Name the blood parasite species.
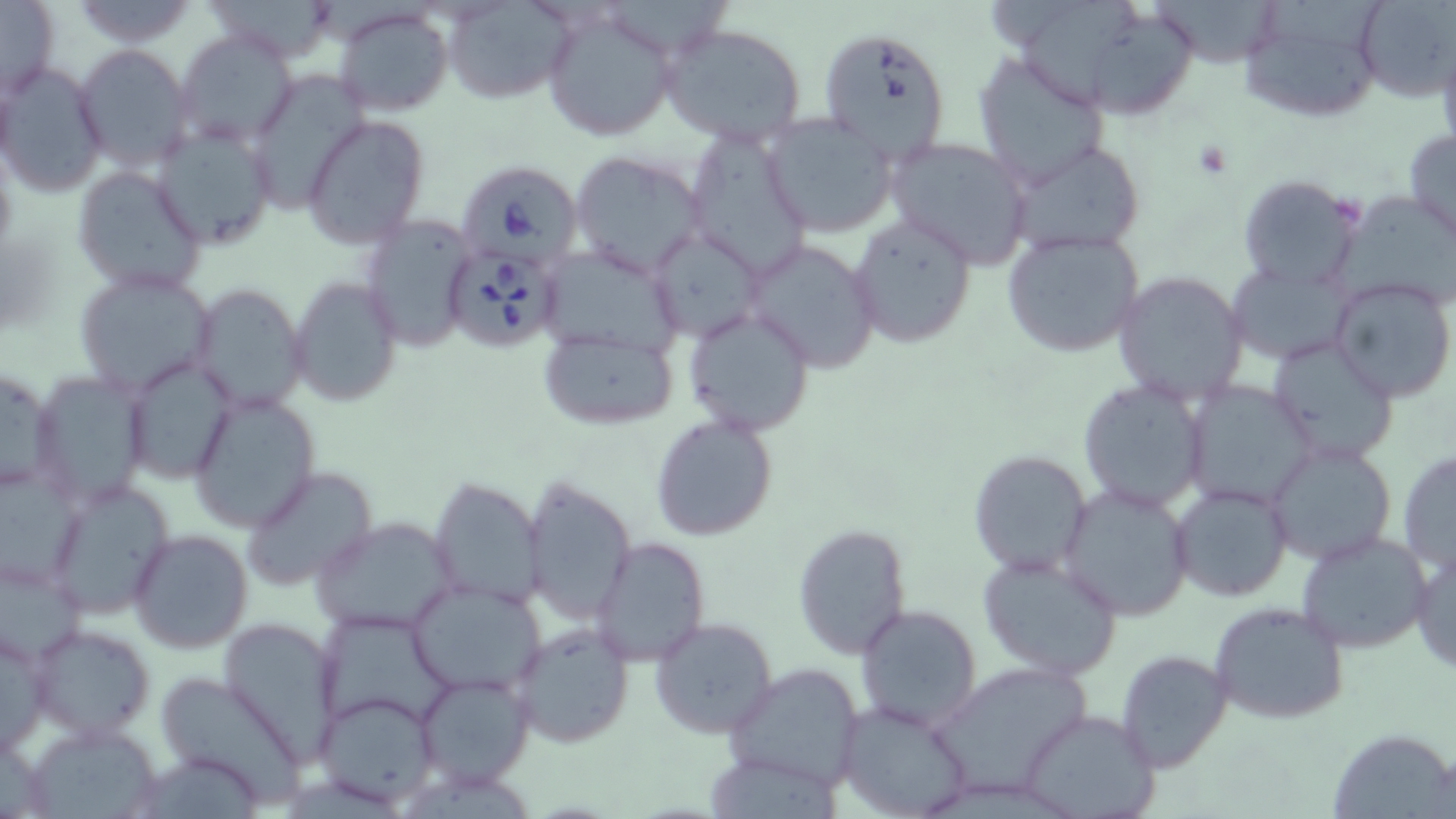
Babesia divergens.

Approximate bounding boxes as (x1,y1)-(x2,y2) corner pairs in pixels. Uninfected red blood cell locations: (204,0)-(334,64), (1145,0)-(1289,68), (1354,0)-(1453,102), (1,1)-(59,100), (68,1)-(199,48), (443,1)-(576,103), (1238,1)-(1391,124), (1026,3)-(1144,110), (542,5)-(679,142), (334,6)-(452,115), (1091,20)-(1194,118), (661,22)-(807,147), (816,24)-(951,161), (174,30)-(302,150), (1437,31)-(1456,167), (73,44)-(192,171), (973,52)-(1109,188), (0,61)-(108,198), (246,72)-(369,214), (761,114)-(896,238), (303,115)-(430,251), (151,120)-(277,249), (684,128)-(811,281), (1404,128)-(1456,243), (885,136)-(1032,267), (1010,139)-(1146,256), (570,149)-(709,276), (73,166)-(205,295), (1234,174)-(1364,293), (1337,190)-(1456,310), (359,212)-(478,353), (846,214)-(979,349), (648,226)-(765,342), (1002,229)-(1145,358), (742,239)-(883,373), (538,243)-(682,362), (1227,259)-(1354,368), (73,268)-(216,396), (1112,270)-(1249,406), (289,275)-(403,406), (1329,275)-(1456,405), (190,284)-(308,411), (683,306)-(816,437), (537,326)-(679,430), (1267,335)-(1402,464), (122,355)-(237,484), (0,363)-(60,497), (32,369)-(151,509), (1078,379)-(1210,513), (1184,380)-(1318,508), (186,389)-(322,533), (649,412)-(779,540), (1265,441)-(1398,568), (1397,448)-(1456,574), (967,449)-(1092,573), (0,462)-(86,592), (242,464)-(378,593), (522,475)-(635,624), (428,477)-(545,606), (44,478)-(174,618), (1169,481)-(1294,604), (1056,482)-(1196,621), (312,516)-(459,637), (794,523)-(911,658), (128,529)-(254,653), (1297,529)-(1434,655), (590,537)-(712,667), (1410,546)-(1456,675), (0,550)-(89,667), (977,551)-(1123,681), (408,580)-(548,696), (1208,601)-(1350,725), (854,604)-(982,731), (315,608)-(455,735), (219,616)-(344,759), (649,616)-(779,741), (510,621)-(636,749), (29,622)-(157,741), (1,627)-(50,754), (1117,650)-(1232,773), (927,660)-(1095,795), (722,661)-(868,790), (152,672)-(309,804), (415,672)-(535,789), (314,691)-(440,808), (836,698)-(977,819), (1017,709)-(1160,819), (22,718)-(167,818), (1328,727)-(1456,817), (708,756)-(839,819). Babesia divergens-infected red blood cell locations: (455,160)-(580,267), (441,244)-(566,352). Optical microscopy. Thin blood film. 1000x magnification. Single field of view. May-Grünwald-Giemsa-stained preparation. Image is 1456×819 pixels.